Locate every Plasmodium parasite.
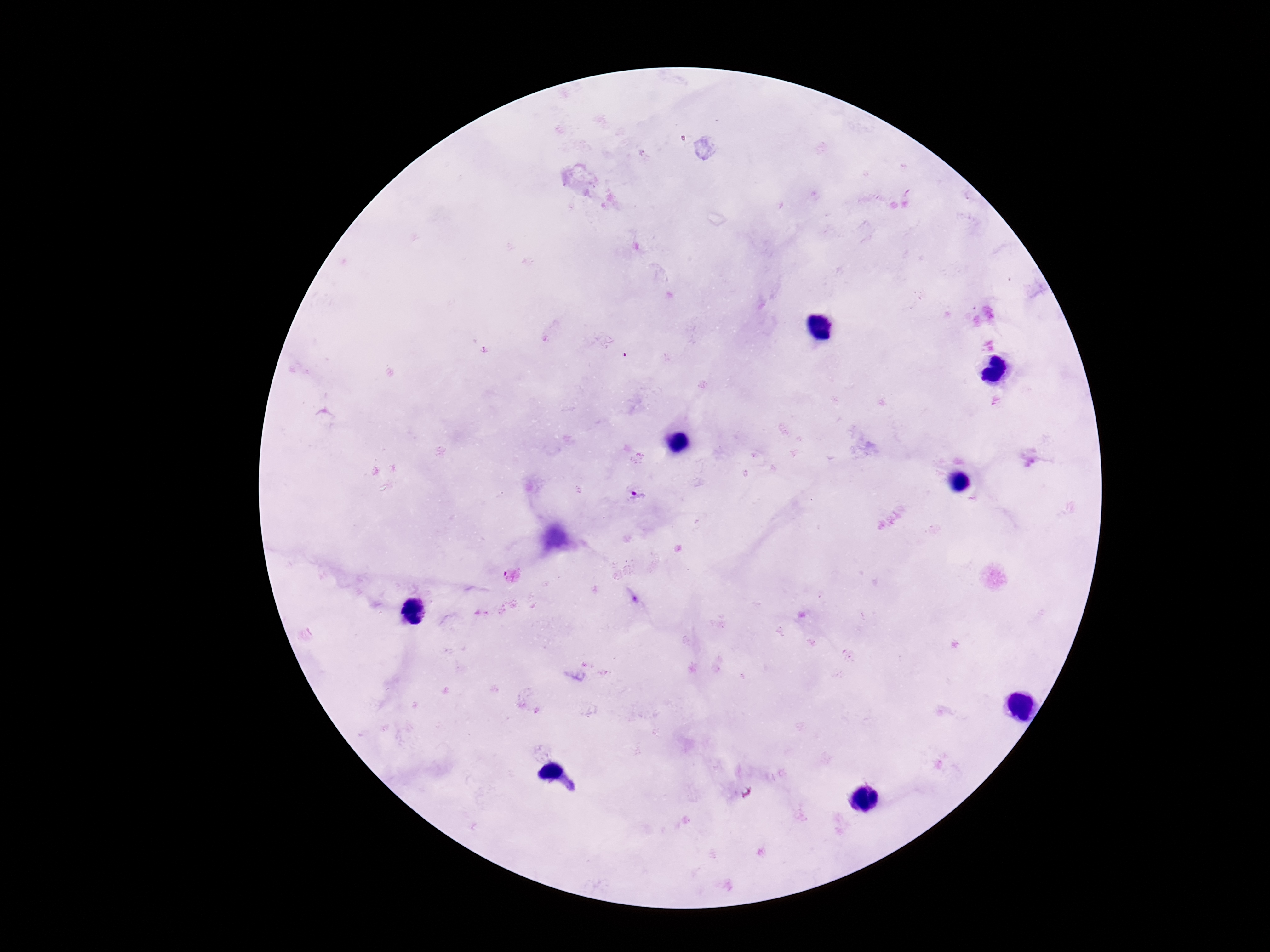

Approximate centers as (x, y) in pixels.
Plasmodium parasites: (635, 496), (512, 575).

magnification = 100x
field of view = one from this slide
capture = smartphone camera through the microscope eyepiece
preparation = thick peripheral-blood smear
stain = Giemsa
patient malaria status = infected
image size = 1270×952 pixels